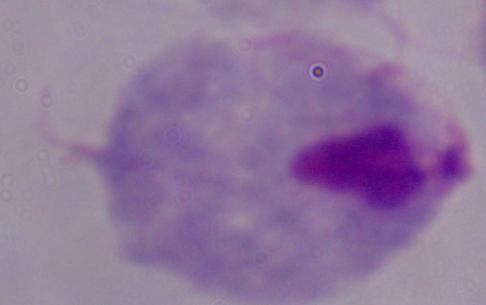

modality = micrograph
magnification = 1000x
identification = trichomonad